State which parasite is depicted.
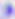

Toxoplasma gondii.

Captured at 400x magnification. Photomicrograph.